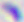
Toxoplasma gondii is shown. Photomicrograph. 400x magnification.